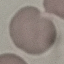
Summary:
  - Malaria status: uninfected
  - Image type: cell patch, automatically extracted from a larger field of view and resized to 64 × 64 pixels
  - Capture: smartphone camera at the microscope eyepiece
  - Stain: Giemsa
  - Preparation: thin blood film